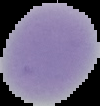 From a thin blood film. The area outside the segmented cell region is set to black. Image is 100×106 pixels. Result: no malaria parasites seen.